Name the cell type shown.
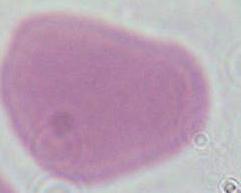

This is an erythrocyte.

modality = photomicrograph
magnification = 1000x